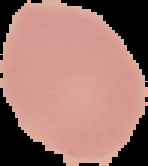

preparation = thin blood film
image type = segmented cell region with the area outside set to black
image size = 148×166 pixels
result = no Plasmodium parasites seen